Name the parasite shown.
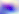
Toxoplasma gondii.

Photomicrograph. Captured at 400x magnification.